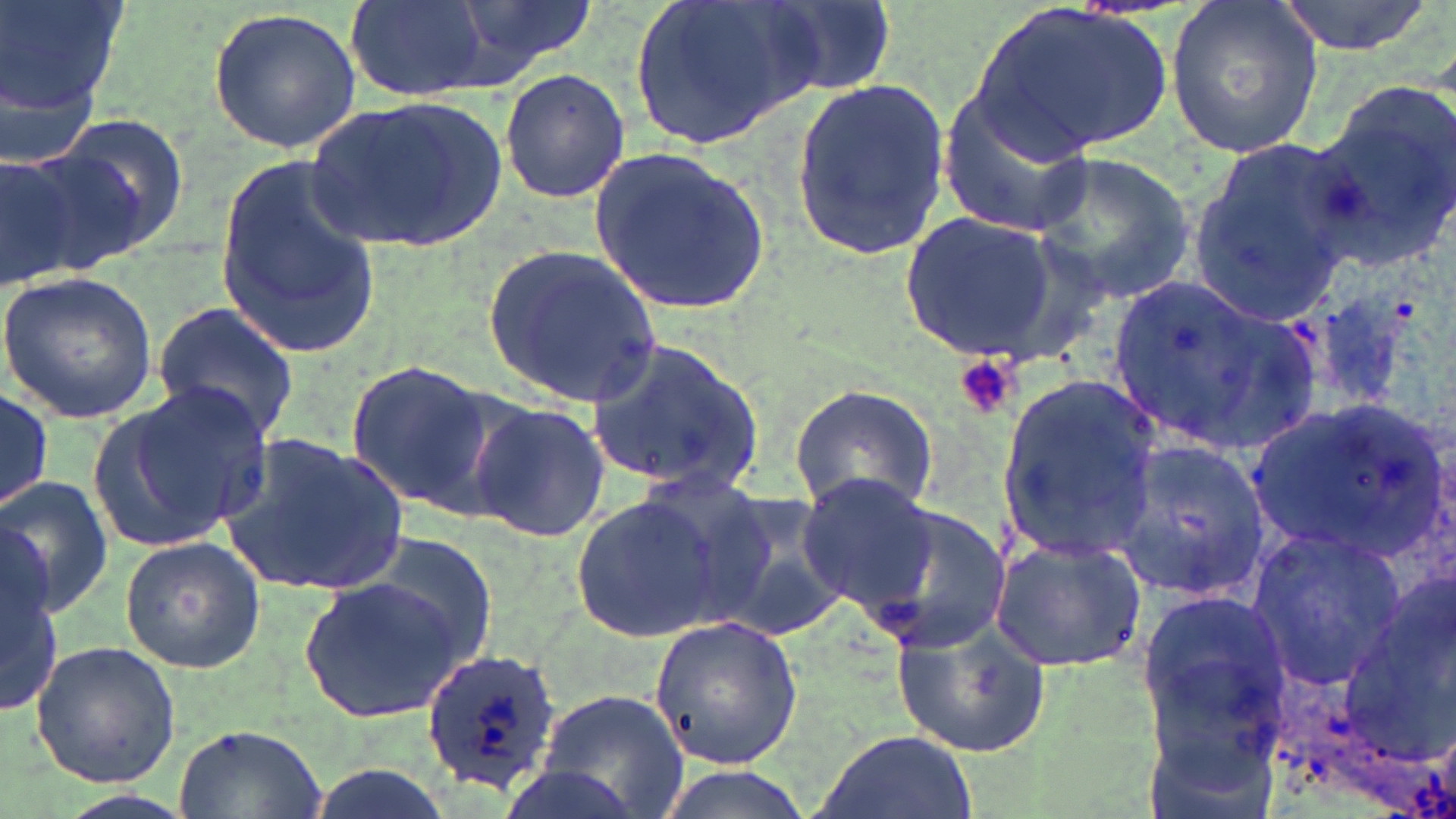 Approximate bounding boxes as named x1/y1/x2/y2 corners in pixels. Uninfected red blood cell locations: (x1=1, y1=0, x2=131, y2=147), (x1=459, y1=0, x2=595, y2=74), (x1=624, y1=0, x2=819, y2=154), (x1=755, y1=0, x2=895, y2=101), (x1=1166, y1=0, x2=1322, y2=159), (x1=1275, y1=0, x2=1436, y2=55), (x1=345, y1=2, x2=491, y2=101), (x1=977, y1=2, x2=1174, y2=157), (x1=208, y1=6, x2=361, y2=154), (x1=499, y1=66, x2=629, y2=205), (x1=789, y1=73, x2=955, y2=263), (x1=1306, y1=84, x2=1456, y2=272), (x1=937, y1=90, x2=1091, y2=237), (x1=304, y1=95, x2=511, y2=251), (x1=51, y1=112, x2=192, y2=257), (x1=11, y1=139, x2=155, y2=278), (x1=588, y1=144, x2=773, y2=316), (x1=1184, y1=144, x2=1357, y2=327), (x1=0, y1=149, x2=89, y2=289), (x1=1031, y1=152, x2=1195, y2=305), (x1=216, y1=156, x2=381, y2=352), (x1=897, y1=210, x2=1064, y2=363), (x1=486, y1=245, x2=663, y2=406), (x1=0, y1=272, x2=159, y2=422), (x1=1104, y1=274, x2=1318, y2=456), (x1=1283, y1=288, x2=1426, y2=429), (x1=150, y1=302, x2=301, y2=442), (x1=585, y1=337, x2=763, y2=499), (x1=343, y1=361, x2=496, y2=514), (x1=997, y1=378, x2=1164, y2=560), (x1=106, y1=380, x2=272, y2=548), (x1=788, y1=383, x2=941, y2=515), (x1=0, y1=385, x2=54, y2=511), (x1=1242, y1=396, x2=1449, y2=569), (x1=471, y1=401, x2=609, y2=542), (x1=219, y1=435, x2=411, y2=597), (x1=1107, y1=436, x2=1273, y2=600), (x1=794, y1=471, x2=940, y2=617), (x1=0, y1=474, x2=113, y2=619), (x1=711, y1=489, x2=851, y2=644), (x1=570, y1=490, x2=724, y2=643), (x1=857, y1=503, x2=1011, y2=653), (x1=1, y1=523, x2=61, y2=710), (x1=1244, y1=523, x2=1408, y2=692), (x1=361, y1=533, x2=501, y2=667), (x1=988, y1=534, x2=1146, y2=673), (x1=119, y1=537, x2=265, y2=672), (x1=1350, y1=563, x2=1456, y2=762), (x1=299, y1=576, x2=469, y2=722), (x1=1135, y1=591, x2=1291, y2=750), (x1=890, y1=611, x2=1050, y2=760), (x1=650, y1=614, x2=803, y2=769), (x1=29, y1=640, x2=182, y2=786), (x1=539, y1=687, x2=690, y2=819), (x1=173, y1=723, x2=329, y2=819), (x1=809, y1=728, x2=978, y2=819), (x1=497, y1=765, x2=641, y2=819). Platelet locations: (x1=952, y1=355, x2=1023, y2=420). Plasmodium ovale-infected red blood cell locations: (x1=423, y1=646, x2=566, y2=799). Slide-level diagnosis: Plasmodium ovale. One field of a larger specimen. Captured at 1000x magnification. Image is 1456×819 pixels. May-Grünwald-Giemsa-stained preparation. Optical microscopy. Thin blood film.